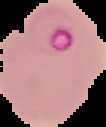

Summary:
  - Preparation: thin blood film
  - Image size: 106×127 pixels
  - Image type: segmented cell region on a black background
  - Malaria status: parasitized